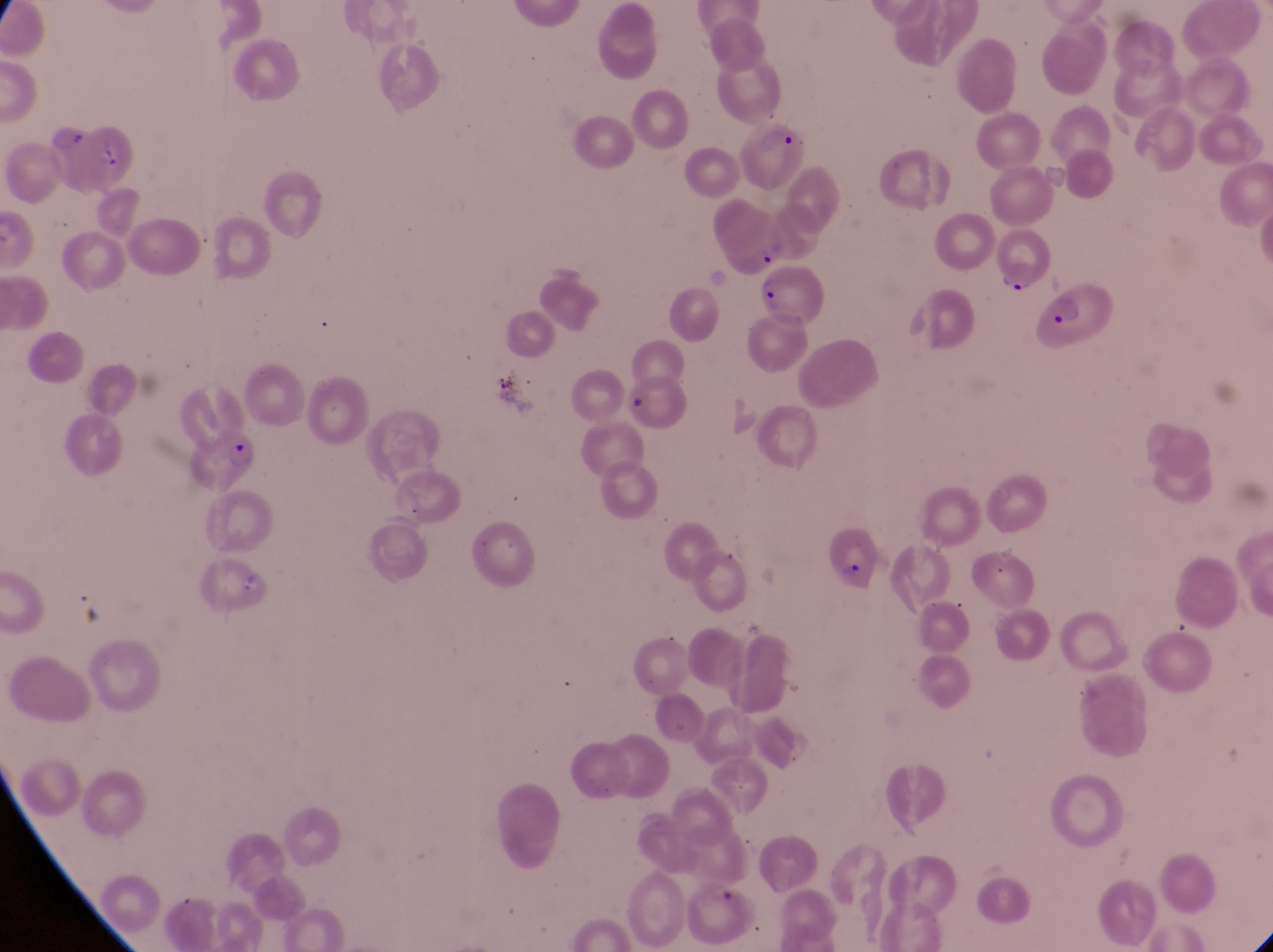

Approximate bounding boxes as (left, top, right, bottom) in pixels. Artifact (platelet-like body, stain precipitate, or debris) locations: (235, 565, 270, 598). Parasitised red blood cell locations: (714, 193, 789, 276), (993, 227, 1060, 294), (762, 270, 824, 332), (1036, 289, 1128, 354), (197, 422, 264, 494), (828, 526, 886, 600). Thin blood film. Image is 1273×952 pixels. Single field of view. Captured by a smartphone held over the eyepiece of an Olympus CX-23 microscope. Collected in Uganda. At a magnification of 1000x.